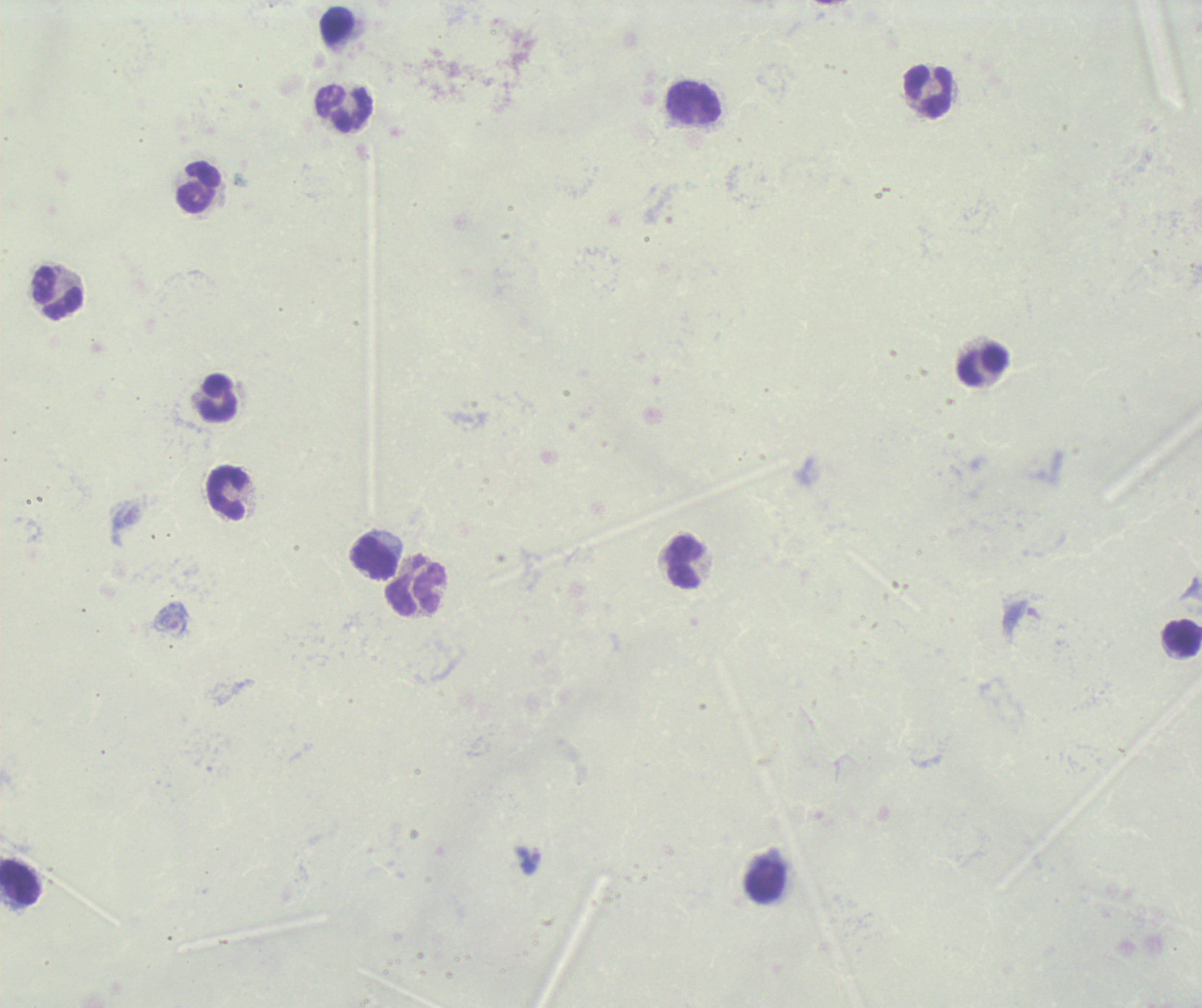
coordinate format = approximate centers as [x, y] in pixels
leukocyte locations = [929, 92], [694, 103], [345, 109], [199, 188], [58, 293], [982, 366], [219, 399], [227, 492], [375, 558], [685, 562], [415, 586], [1183, 638], [766, 880], [20, 883]
trophozoite locations = [529, 860]
preparation = thick smear of blood
result = positive for Plasmodium parasites
background quality = unsatisfactory
image size = 1202×1008 pixels
field of view = single
magnification = 100x
stain = Romanowsky
context = previously used in a real diagnosis